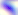

Summary:
  - Magnification: 400x
  - Modality: micrograph
  - Identification: Toxoplasma gondii